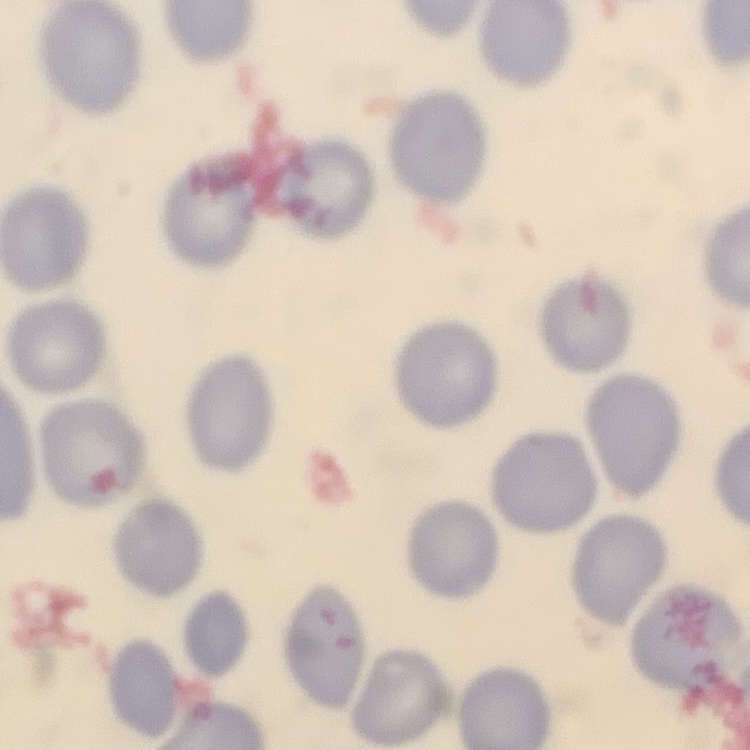 The erythrocytes show no rouleaux formation. Field's or Giemsa stain. Square crop of a larger photomicrograph. Thin blood film.